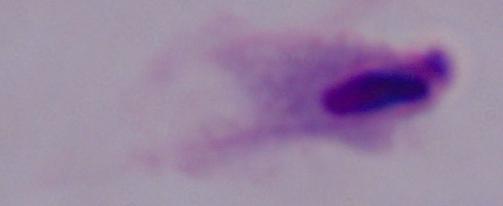

magnification = 1000x
modality = photomicrograph
identification = trichomonad